Assess this cell for malaria.
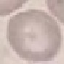
It is uninfected.

Thin blood film. Giemsa-stained preparation. Automatically extracted cell patch, resized to 64 × 64 pixels. Photographed with a smartphone camera at the microscope eyepiece.